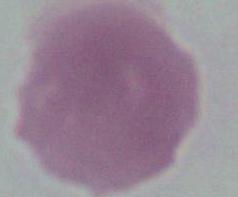
magnification = 1000x
modality = photomicrograph
identification = erythrocyte